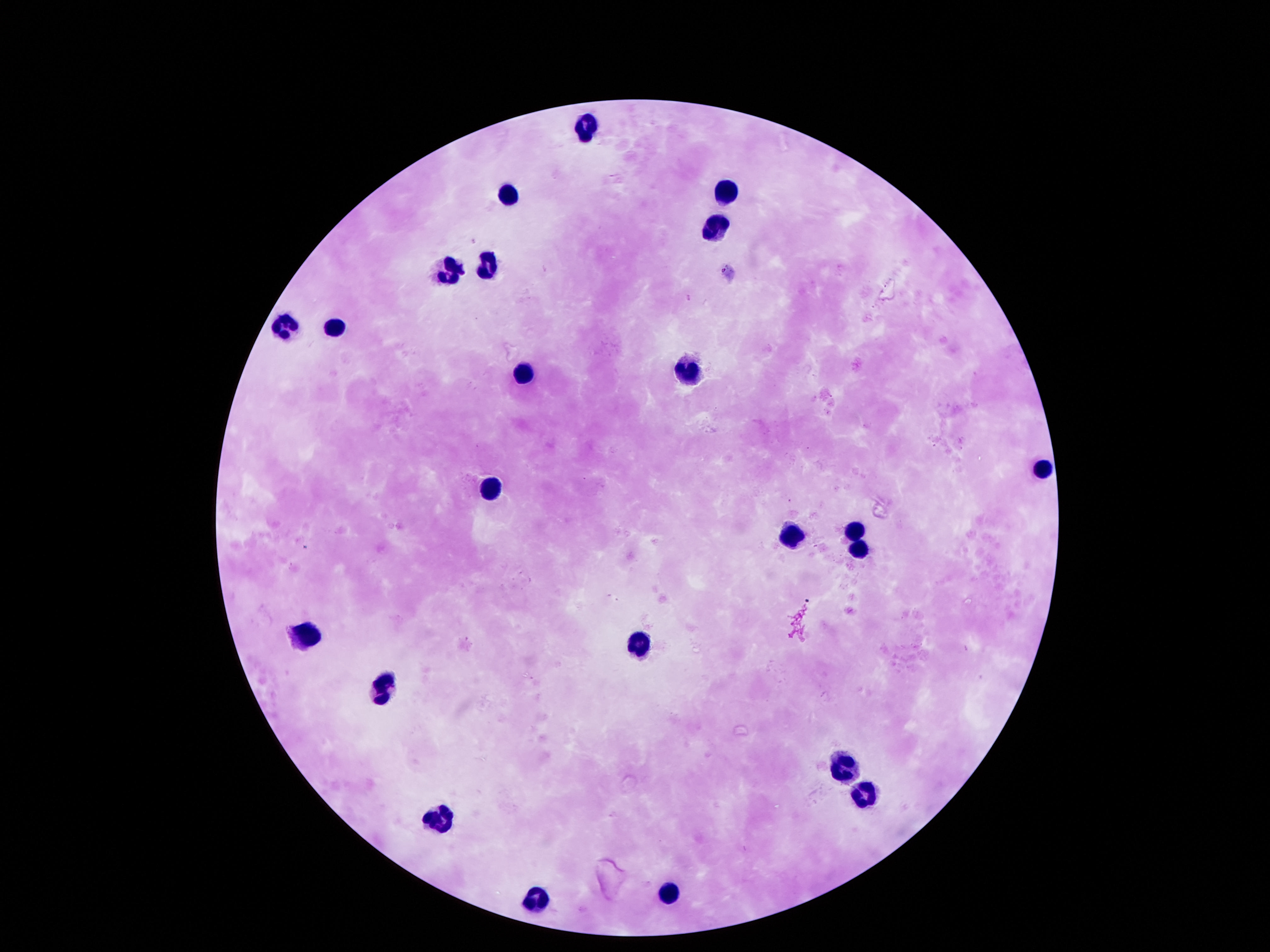

Approximate object centers, in pixels from the top-left corner.
Summary:
  - Leukocyte locations: (x=584, y=118), (x=726, y=186), (x=506, y=190), (x=713, y=225), (x=484, y=262), (x=448, y=267), (x=280, y=322), (x=335, y=323), (x=687, y=370), (x=516, y=371), (x=1039, y=465), (x=493, y=484), (x=855, y=530), (x=790, y=532), (x=858, y=546), (x=306, y=636), (x=639, y=641), (x=377, y=681), (x=839, y=762), (x=861, y=791), (x=438, y=820), (x=664, y=885), (x=535, y=898)
  - Patient malaria status: negative
  - Capture: smartphone camera through the microscope eyepiece
  - Stain: Giemsa
  - Preparation: thick blood smear
  - Field of view: single
  - Magnification: 100x
  - Image size: 1270×952 pixels